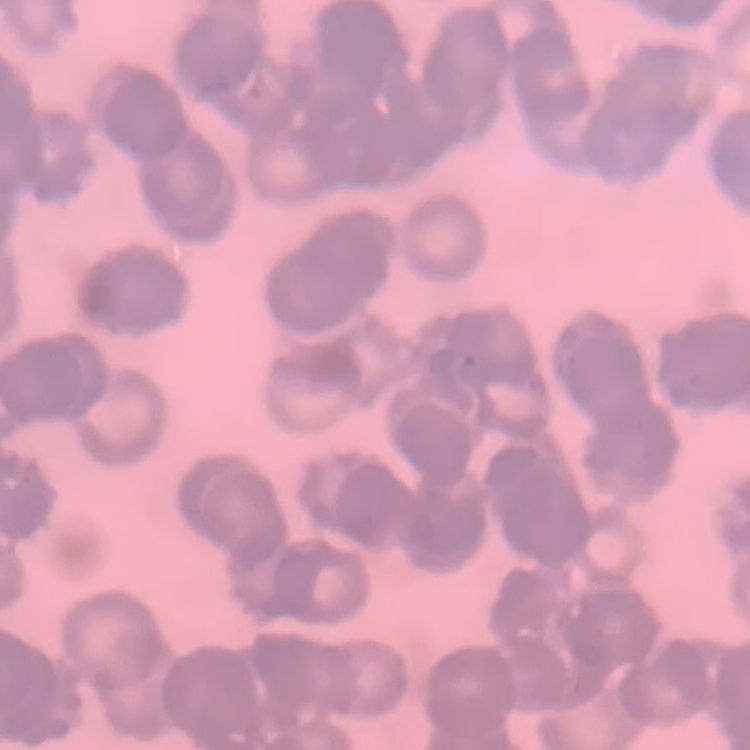

The erythrocytes exhibit rouleaux formation. Thin blood film. Stained with either Field's or Giemsa. One tile cut from a larger photomicrograph.